Assess the morphology of the red blood cells.
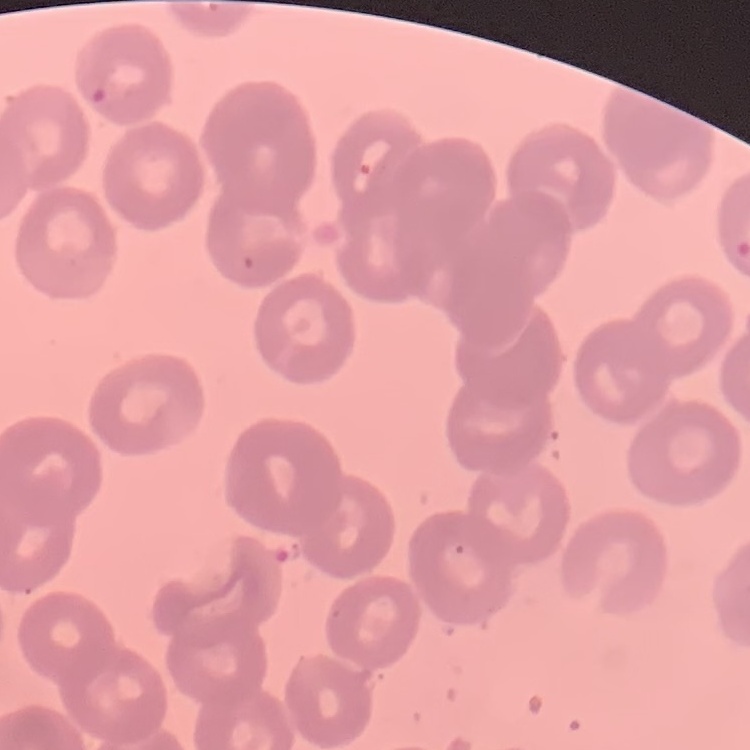
They show no rouleaux formation.

Square crop of a larger photomicrograph. Field's or Giemsa stain. Thin blood film.